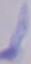

A trypanosome is seen. Captured at 1000x magnification. Photomicrograph.